Mark where platelets are.
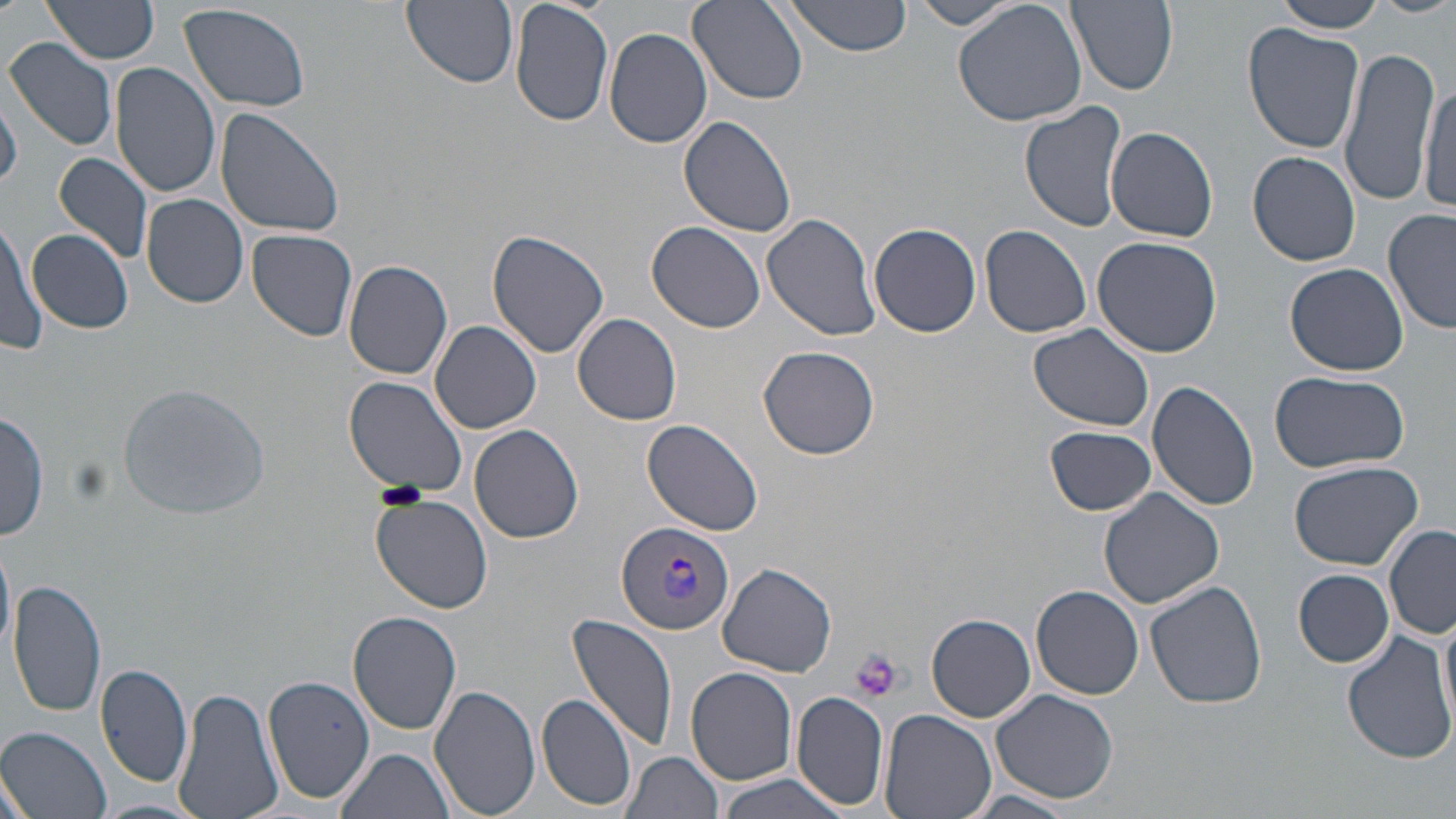
Approximate bounding boxes as [x1, y1, x2, y2] in pixels.
Platelets: [377, 482, 429, 509], [847, 648, 903, 702].

Summary:
  - Plasmodium vivax-infected red blood cell locations: [615, 519, 734, 636]
  - Uninfected red blood cell locations: [41, 0, 161, 68], [402, 0, 519, 89], [510, 0, 613, 127], [784, 0, 915, 56], [952, 0, 1088, 128], [1067, 0, 1179, 94], [1272, 0, 1387, 35], [1374, 0, 1456, 17], [688, 1, 809, 105], [908, 1, 1023, 31], [176, 2, 313, 113], [1243, 23, 1364, 154], [605, 26, 713, 148], [6, 36, 118, 152], [1338, 46, 1441, 207], [110, 63, 221, 198], [1419, 76, 1456, 216], [1, 92, 23, 190], [1020, 101, 1127, 232], [216, 106, 346, 240], [679, 116, 798, 240], [1106, 126, 1218, 242], [1248, 151, 1361, 266], [55, 152, 153, 265], [142, 193, 249, 310], [1383, 209, 1455, 335], [762, 212, 880, 343], [0, 217, 45, 355], [646, 220, 767, 333], [869, 222, 981, 337], [979, 224, 1092, 338], [26, 228, 133, 335], [247, 229, 358, 344], [488, 229, 612, 359], [1091, 235, 1223, 356], [344, 259, 454, 380], [1285, 263, 1409, 375], [572, 312, 682, 425], [430, 321, 541, 433], [1028, 323, 1155, 431], [758, 345, 880, 460], [1268, 371, 1407, 472], [344, 376, 469, 498], [1149, 379, 1259, 512], [1, 410, 49, 542], [641, 417, 766, 537], [470, 424, 583, 543], [1044, 425, 1158, 516], [1287, 459, 1425, 569], [1098, 488, 1223, 608], [372, 494, 494, 613], [1385, 527, 1456, 639], [0, 540, 14, 667], [718, 562, 837, 679], [1294, 568, 1393, 668], [9, 577, 108, 719], [1145, 579, 1269, 708], [1032, 584, 1144, 698], [1438, 607, 1456, 734], [348, 612, 462, 735], [567, 613, 681, 753], [927, 613, 1037, 722], [1342, 628, 1456, 764], [96, 662, 192, 790], [684, 666, 798, 787], [262, 673, 375, 806], [428, 683, 542, 817], [174, 685, 283, 819], [989, 687, 1119, 804], [791, 690, 890, 810], [536, 693, 638, 810], [880, 708, 997, 819], [0, 727, 112, 818], [335, 746, 456, 819], [620, 751, 723, 819], [0, 770, 34, 819], [713, 773, 852, 818], [959, 790, 1079, 818], [93, 798, 212, 819]
  - Slide-level diagnosis: Plasmodium vivax
  - Modality: optical microscopy
  - Preparation: thin blood smear
  - Stain: May-Grünwald-Giemsa
  - Field of view: one of a larger specimen
  - Magnification: 1000x
  - Image size: 1456×819 pixels